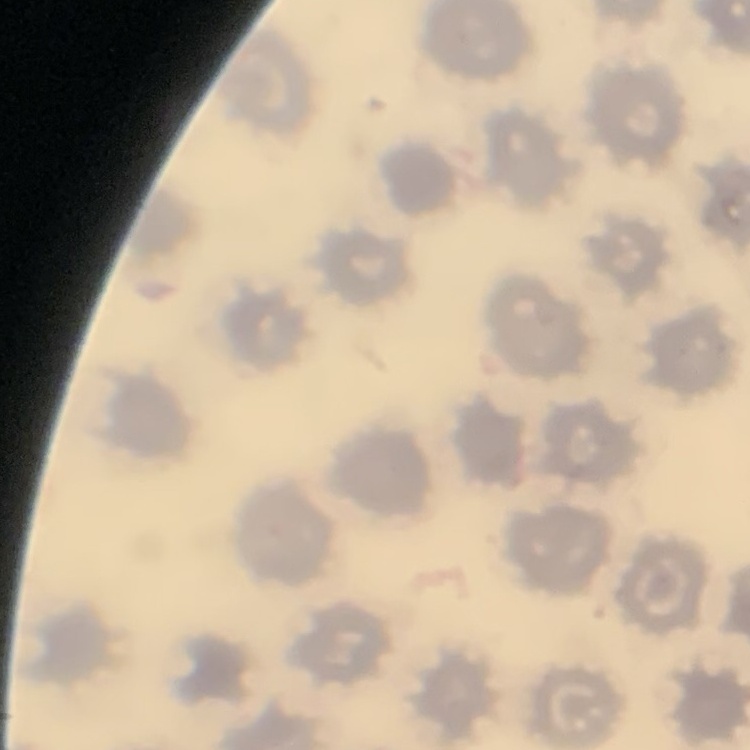

red blood cell morphology = no rouleaux formation
preparation = thin blood smear
stain = Field's or Giemsa
image type = square crop of a larger photomicrograph